Describe the morphology of the red blood cells.
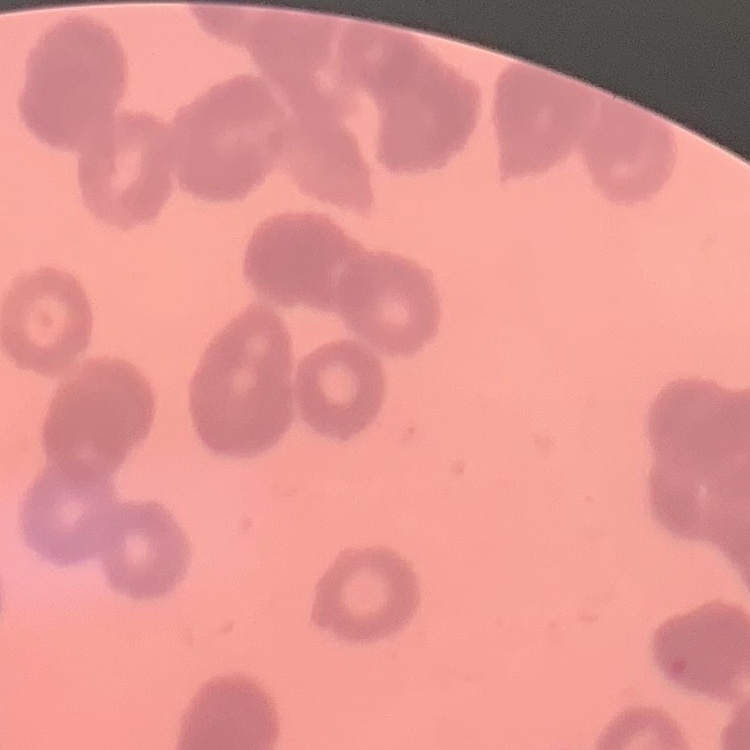
Rouleaux formation.

image type = square crop of a larger photomicrograph
stain = Field's or Giemsa
preparation = thin blood smear